Outline platelets.
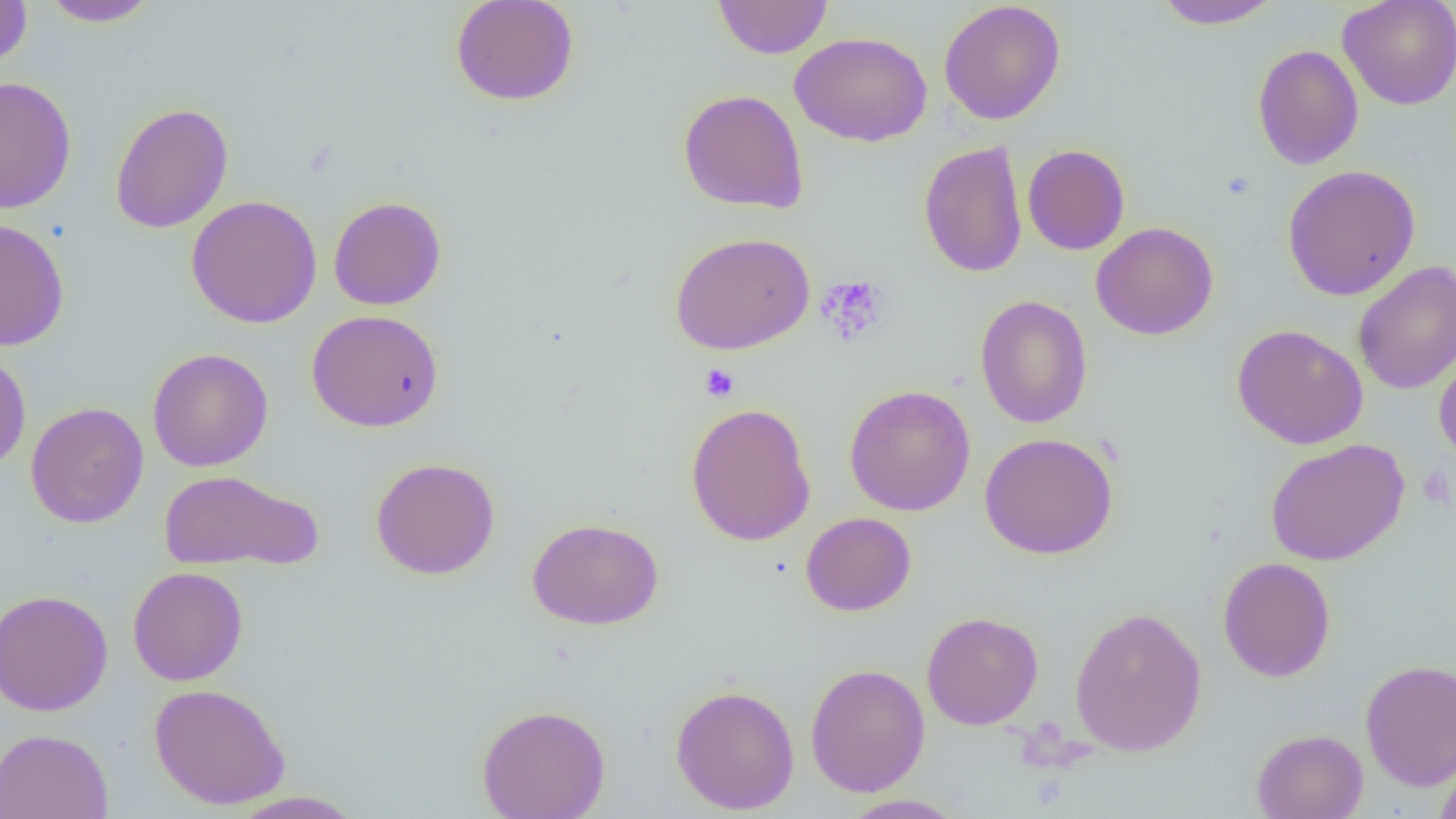
Approximate bounding boxes as (x1,y1)-(x2,y2) corner pairs in pixels.
Platelets: (816,276)-(890,347), (700,363)-(740,402), (1416,466)-(1454,509).

Uninfected red blood cell locations: (38,0)-(161,27), (450,0)-(580,106), (713,0)-(833,59), (1151,0)-(1284,30), (1338,0)-(1456,110), (0,1)-(33,67), (938,1)-(1066,125), (789,31)-(932,147), (1252,44)-(1363,170), (1,76)-(77,213), (678,89)-(809,214), (109,101)-(234,234), (918,140)-(1028,278), (1022,144)-(1130,256), (1282,164)-(1420,301), (185,195)-(322,328), (328,196)-(447,311), (0,218)-(69,351), (1091,222)-(1218,340), (669,231)-(815,355), (1353,260)-(1456,395), (975,295)-(1092,429), (306,310)-(444,432), (1232,323)-(1368,449), (1434,347)-(1456,468), (148,348)-(273,471), (0,350)-(31,471), (844,385)-(976,516), (25,401)-(149,528), (685,402)-(816,547), (979,432)-(1118,559), (1265,438)-(1409,565), (371,457)-(500,579), (159,469)-(323,574), (800,512)-(916,616), (527,517)-(664,630), (1218,556)-(1336,683), (128,567)-(248,686), (0,589)-(113,716), (1069,606)-(1207,757), (921,611)-(1043,730), (1359,659)-(1456,791), (804,663)-(930,797), (149,683)-(290,810), (670,684)-(799,815), (476,704)-(611,819), (0,728)-(114,819), (1252,728)-(1369,818), (1434,759)-(1456,819), (225,790)-(368,818), (839,794)-(967,818). Slide-level diagnosis: no evidence of blood parasites. Thin blood film. Image is 1456×819 pixels. Light microscopy. 1000x magnification. Single field of view.